Report the malaria status of this cell.
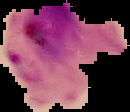

Parasitized.

Summary:
  - Image size: 130×112 pixels
  - Preparation: thin blood film
  - Image type: cell region segmented out of the field of view; surrounding area masked to black